Name the parasite shown.
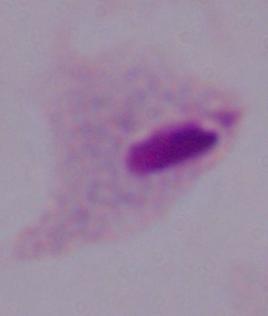
This is a trichomonad.

{
  "modality": "photomicrograph",
  "magnification": "1000x"
}